Name the blood parasite species.
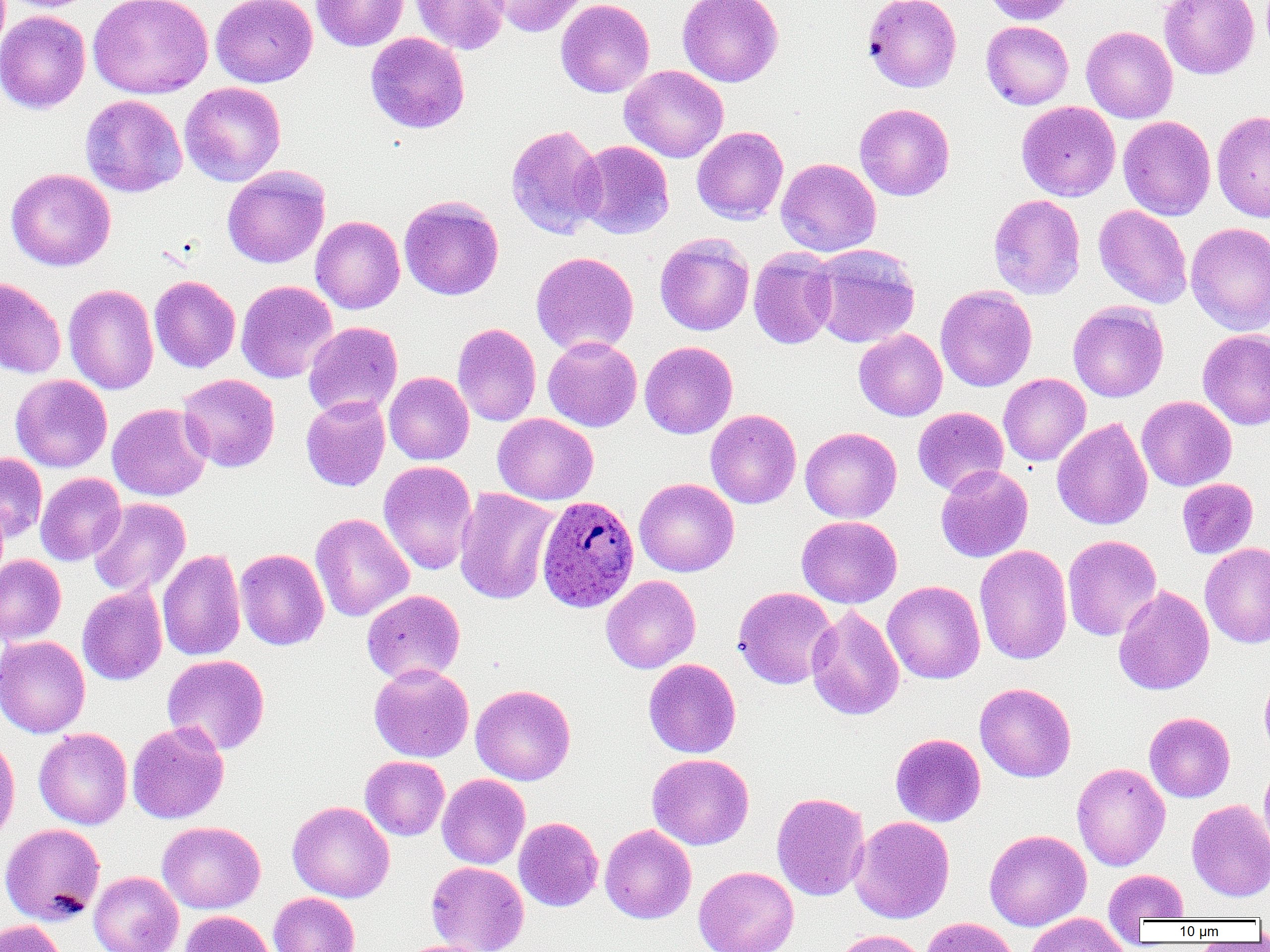

Plasmodium ovale.

{
  "magnification": "1000x",
  "field_of_view": "one of a larger specimen",
  "image_size": "1270×952 pixels",
  "plasmodium_ovale_infected_red_blood_cell_locations": "approximate bounding boxes as (x1,y1)-(x2,y2) corner pairs in pixels: (537,495)-(640,612)",
  "uninfected_red_blood_cell_locations": "approximate bounding boxes as (x1,y1)-(x2,y2) corner pairs in pixels: (1,0)-(99,13), (88,0)-(213,99), (211,0)-(318,87), (311,0)-(408,51), (411,0)-(510,55), (488,0)-(588,37), (556,0)-(655,97), (677,0)-(783,87), (863,0)-(962,92), (984,0)-(1077,26), (1159,0)-(1260,79), (1,10)-(91,114), (981,21)-(1074,110), (1081,26)-(1178,123), (365,32)-(470,134), (619,65)-(728,163), (180,82)-(286,186), (79,94)-(187,197), (1017,101)-(1120,201), (855,103)-(955,201), (1212,110)-(1270,222), (1118,115)-(1216,220), (506,123)-(606,239), (692,126)-(788,224), (574,140)-(675,239), (776,158)-(881,257), (223,165)-(330,268), (6,168)-(116,271), (988,194)-(1086,300), (399,195)-(504,300), (1093,204)-(1192,308), (311,216)-(405,314), (1185,221)-(1270,336), (655,232)-(754,336), (811,244)-(920,348), (748,246)-(838,349), (531,251)-(639,357), (149,275)-(241,373), (0,277)-(67,379), (236,280)-(338,383), (63,284)-(159,395), (935,285)-(1037,392), (1068,302)-(1168,402), (303,322)-(403,419), (452,323)-(541,426), (854,329)-(947,421), (1198,329)-(1270,430), (543,336)-(642,432), (640,341)-(738,439), (384,372)-(474,465), (178,373)-(280,472), (998,373)-(1091,466), (11,374)-(112,472), (301,396)-(390,491), (1137,396)-(1236,491), (107,403)-(212,501), (913,407)-(1008,496), (705,409)-(801,509), (493,413)-(598,505), (1052,417)-(1152,530), (705,422)-(898,512), (800,427)-(901,523), (0,453)-(47,542), (378,461)-(477,575), (935,464)-(1033,562), (35,472)-(126,566), (634,478)-(739,577), (1177,478)-(1258,559), (454,487)-(559,605), (88,498)-(191,597), (311,513)-(414,622), (796,516)-(902,608), (1062,534)-(1162,641), (1200,542)-(1270,649), (974,544)-(1073,665), (157,549)-(245,661), (235,549)-(329,650), (0,555)-(66,645), (884,569)-(1072,671), (601,575)-(700,673), (883,581)-(985,684), (77,585)-(168,685), (1114,585)-(1215,696), (733,586)-(838,689), (361,589)-(466,684), (806,605)-(904,720), (0,636)-(90,738), (162,654)-(270,755), (643,658)-(741,758), (369,663)-(474,763), (1259,673)-(1270,758), (974,682)-(1076,782), (470,684)-(575,785), (1145,712)-(1235,802), (127,721)-(229,823), (33,728)-(132,829), (890,733)-(986,827), (0,734)-(20,849), (647,753)-(754,850), (361,756)-(449,840), (1072,762)-(1170,871), (1258,763)-(1270,856), (437,773)-(530,869), (771,792)-(870,901), (1187,799)-(1270,902), (287,800)-(394,903), (850,816)-(955,923), (514,817)-(603,911), (157,821)-(265,913), (0,823)-(105,926), (600,824)-(696,924), (984,829)-(1092,930), (426,861)-(530,952), (693,865)-(799,952), (1103,869)-(1189,922), (89,871)-(184,952), (268,892)-(359,952), (180,910)-(275,952), (1024,913)-(1131,952), (921,917)-(1021,952), (0,919)-(66,952), (832,929)-(929,952), (395,940)-(493,952)",
  "preparation": "thin blood film",
  "modality": "light microscopy"
}